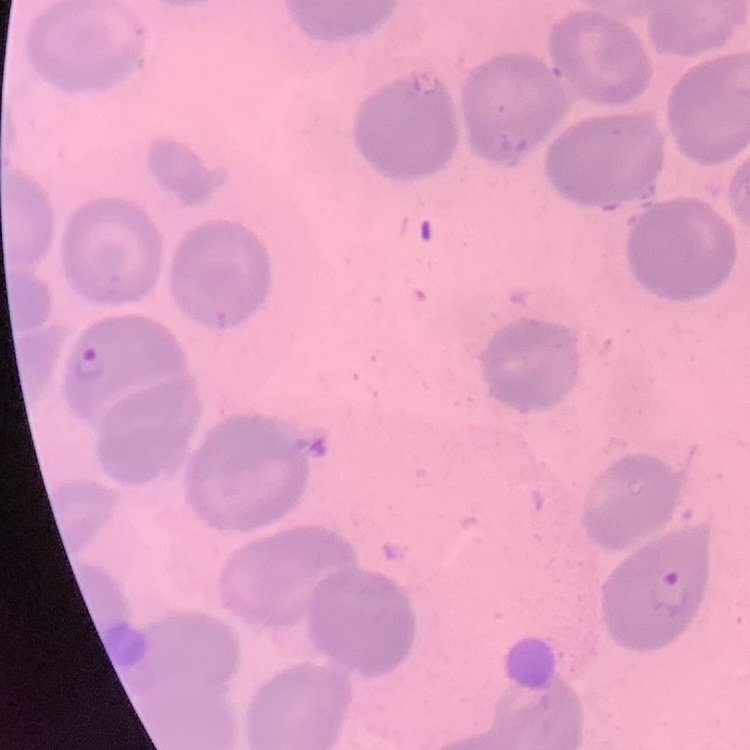

erythrocyte morphology = no rouleaux formation
image type = one tile cut from a larger photomicrograph
stain = Field's or Giemsa
preparation = thin blood film